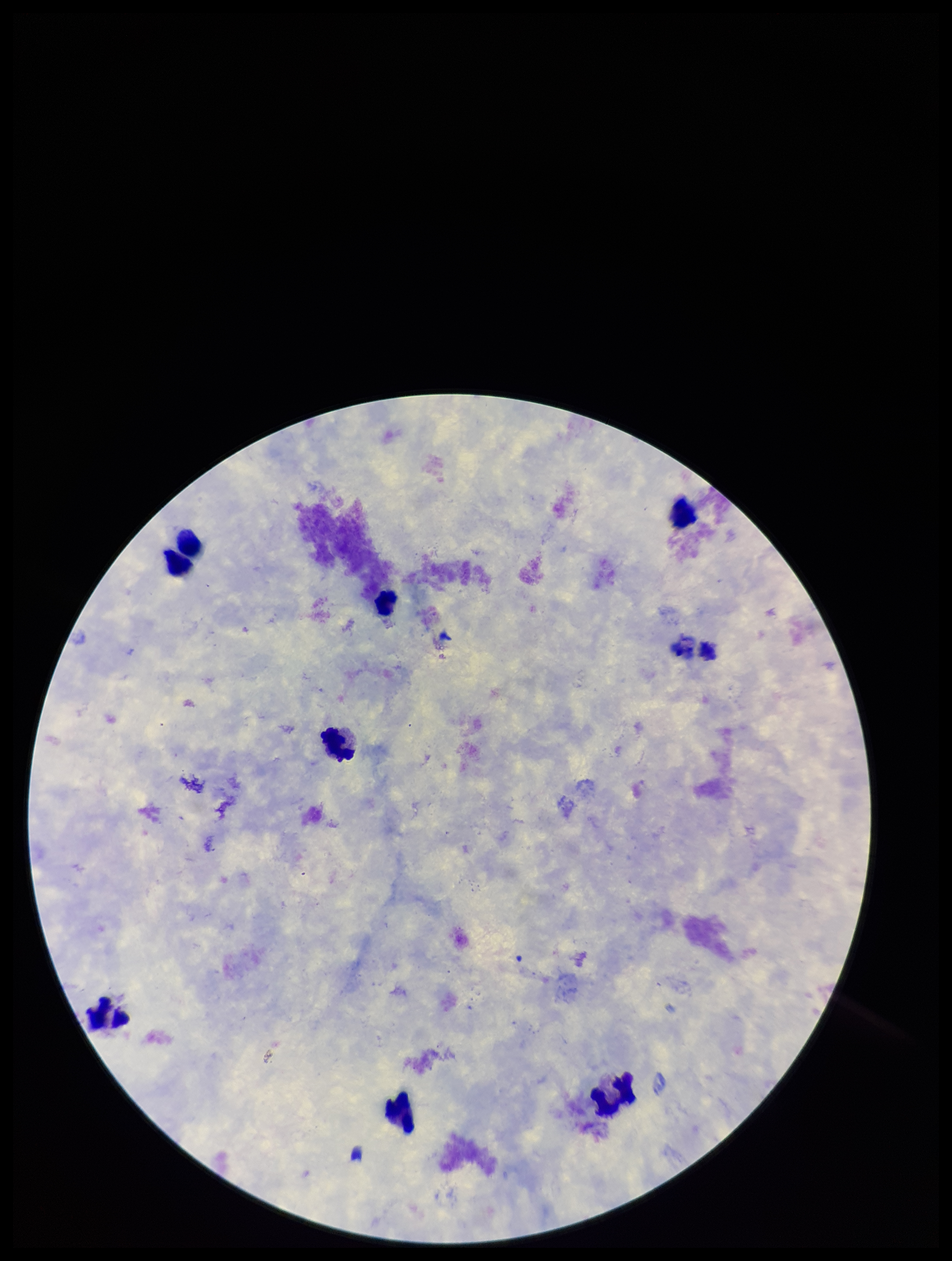
{
  "leukocyte_count": 7,
  "preparation": "thick smear",
  "capture": "smartphone photograph through the microscope eyepiece",
  "parasite_count": 0,
  "image_size": "952×1261 pixels",
  "plasmodium_parasites": "none seen",
  "patient_malaria_status": "negative",
  "stain": "Giemsa",
  "field_of_view": "one from this slide"
}